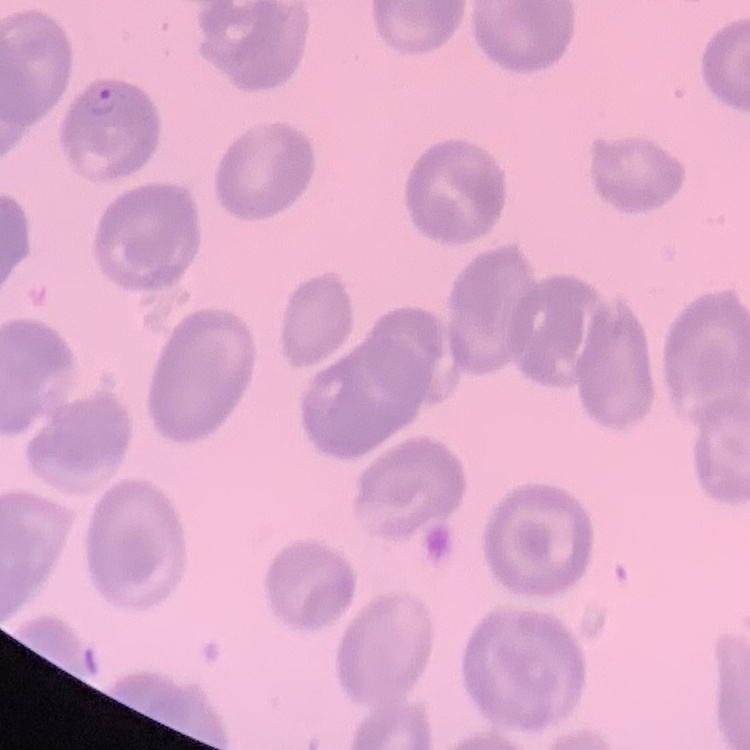

{
  "red_blood_cell_morphology": "no rouleaux formation",
  "image_type": "square crop of a larger photomicrograph",
  "stain": "Field's or Giemsa",
  "preparation": "thin blood film"
}